Locate every malaria parasite.
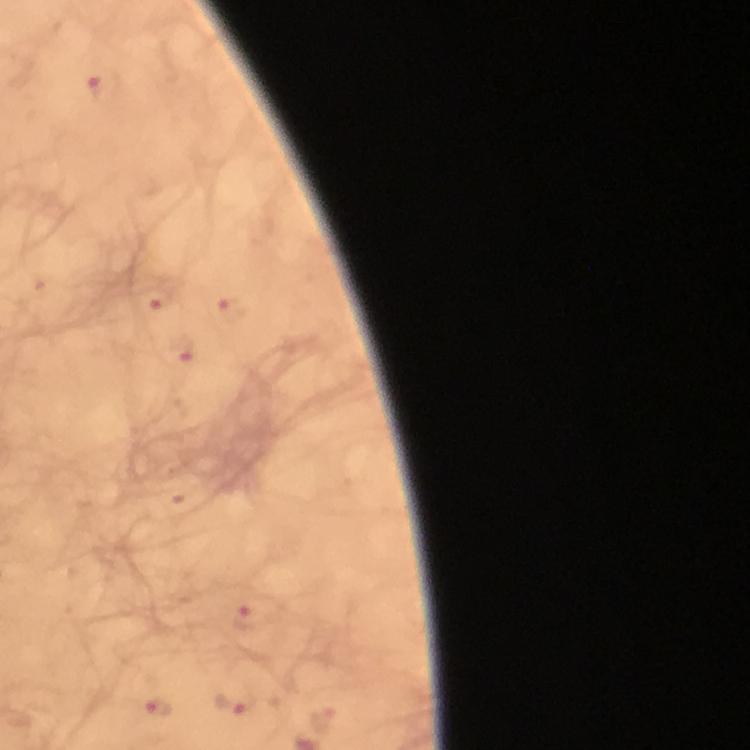

Approximate centers as {x, y} in pixels.
Malaria parasites: {105, 87}, {153, 299}, {232, 309}, {182, 351}, {249, 616}, {235, 705}, {159, 708}, {323, 718}.

Summary:
  - Preparation: thick smear
  - Image size: 750×750 pixels
  - Context: from a malaria diagnostic workup
  - Stain: Giemsa
  - Magnification: 100x
  - Capture: smartphone camera through the microscope
  - Immersion oil: applied
  - Cropped from: one field of view